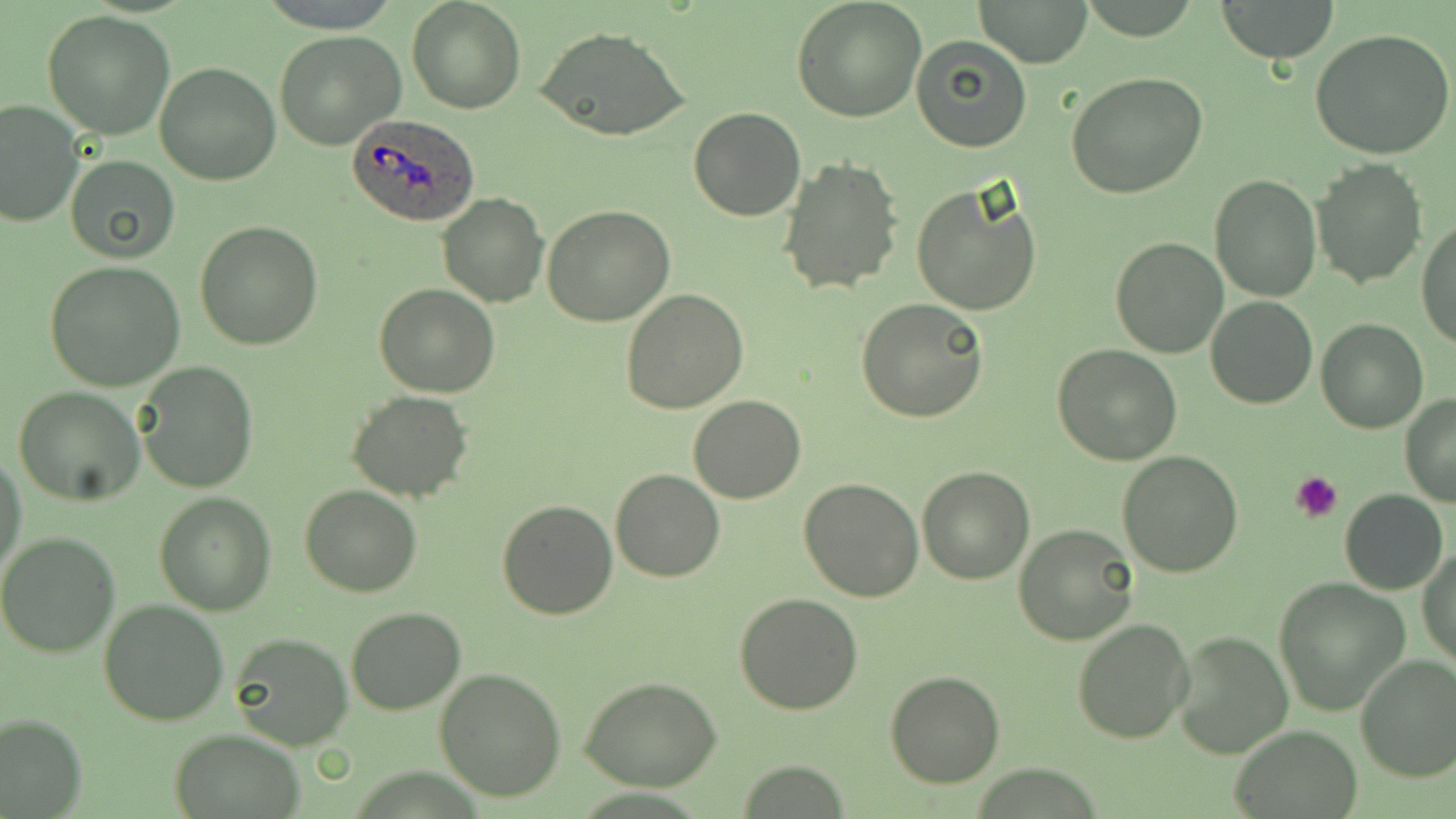

Summary:
  - Coordinate format: approximate bounding boxes as named x1/y1/x2/y2 corners in pixels
  - Uninfected red blood cell locations: (x1=407, y1=0, x2=524, y2=114), (x1=793, y1=0, x2=927, y2=122), (x1=976, y1=0, x2=1092, y2=68), (x1=1215, y1=0, x2=1341, y2=62), (x1=42, y1=10, x2=177, y2=140), (x1=534, y1=26, x2=690, y2=144), (x1=1310, y1=28, x2=1456, y2=161), (x1=274, y1=29, x2=406, y2=150), (x1=911, y1=36, x2=1032, y2=152), (x1=153, y1=61, x2=281, y2=185), (x1=1066, y1=71, x2=1208, y2=198), (x1=0, y1=100, x2=82, y2=228), (x1=688, y1=107, x2=808, y2=221), (x1=64, y1=155, x2=180, y2=262), (x1=775, y1=158, x2=904, y2=296), (x1=1313, y1=159, x2=1426, y2=288), (x1=1210, y1=175, x2=1320, y2=300), (x1=911, y1=181, x2=1044, y2=317), (x1=437, y1=191, x2=550, y2=307), (x1=541, y1=206, x2=675, y2=327), (x1=1416, y1=218, x2=1456, y2=350), (x1=194, y1=221, x2=322, y2=352), (x1=1111, y1=235, x2=1229, y2=357), (x1=46, y1=260, x2=185, y2=391), (x1=374, y1=283, x2=500, y2=398), (x1=621, y1=288, x2=749, y2=412), (x1=1205, y1=295, x2=1318, y2=408), (x1=858, y1=299, x2=989, y2=423), (x1=1316, y1=319, x2=1429, y2=435), (x1=1051, y1=343, x2=1182, y2=466), (x1=137, y1=364, x2=258, y2=492), (x1=13, y1=386, x2=147, y2=506), (x1=347, y1=390, x2=474, y2=501), (x1=687, y1=395, x2=806, y2=504), (x1=1399, y1=395, x2=1456, y2=507), (x1=1116, y1=450, x2=1244, y2=577), (x1=1, y1=451, x2=28, y2=583), (x1=917, y1=466, x2=1035, y2=584), (x1=611, y1=469, x2=724, y2=582), (x1=799, y1=479, x2=924, y2=602), (x1=299, y1=486, x2=423, y2=597), (x1=1341, y1=490, x2=1448, y2=595), (x1=153, y1=491, x2=278, y2=614), (x1=497, y1=500, x2=619, y2=621), (x1=1014, y1=523, x2=1140, y2=645), (x1=0, y1=532, x2=120, y2=659), (x1=1418, y1=543, x2=1455, y2=671), (x1=1274, y1=577, x2=1408, y2=714), (x1=733, y1=593, x2=863, y2=715), (x1=98, y1=599, x2=229, y2=726), (x1=345, y1=606, x2=467, y2=714), (x1=1071, y1=616, x2=1195, y2=743), (x1=1170, y1=631, x2=1293, y2=760), (x1=227, y1=633, x2=352, y2=749), (x1=1355, y1=654, x2=1456, y2=782), (x1=433, y1=667, x2=567, y2=802), (x1=884, y1=672, x2=1004, y2=788), (x1=580, y1=677, x2=722, y2=790), (x1=0, y1=714, x2=85, y2=818), (x1=1232, y1=726, x2=1360, y2=818), (x1=169, y1=729, x2=301, y2=819)
  - Platelet locations: (x1=1291, y1=469, x2=1346, y2=520)
  - Plasmodium ovale-infected red blood cell locations: (x1=344, y1=115, x2=481, y2=226)
  - Slide-level diagnosis: Plasmodium ovale
  - Stain: May-Grünwald-Giemsa
  - Field of view: single
  - Preparation: thin blood smear
  - Modality: light microscopy
  - Image size: 1456×819 pixels
  - Magnification: 1000x